Describe the morphology of the red blood cells.
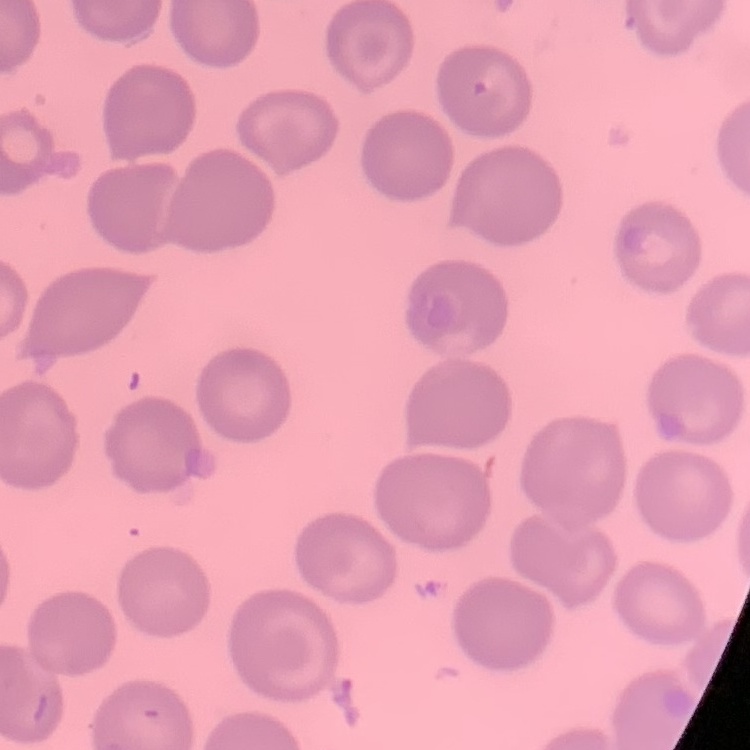

They show no rouleaux formation.

Summary:
  - Image type: square crop of a larger photomicrograph
  - Preparation: thin blood smear
  - Stain: Field's or Giemsa